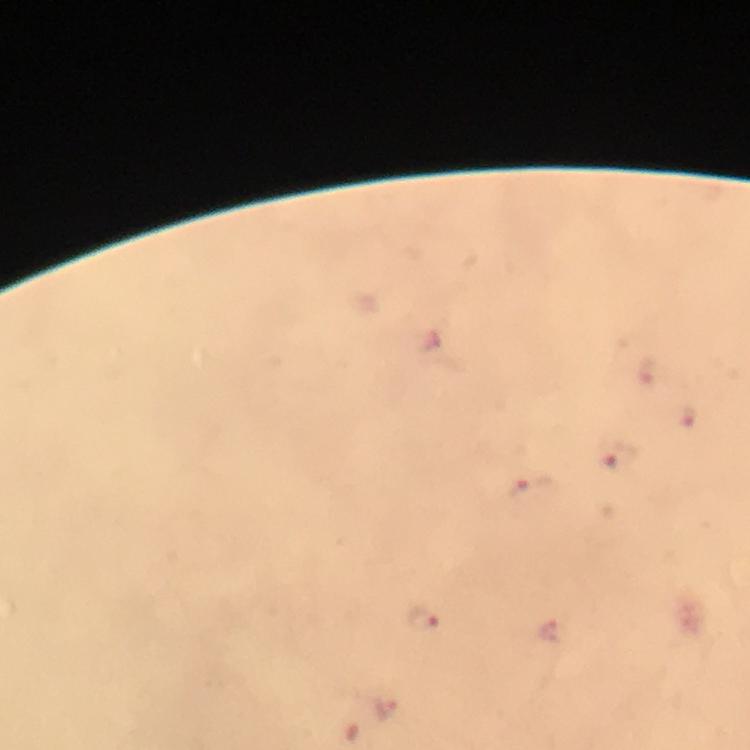

context = from a malaria diagnostic workup
magnification = 100x
capture = smartphone mounted on the microscope
image size = 750×750 pixels
immersion oil = applied
preparation = thick blood smear
cropped from = a single field of view
malaria parasite locations = approximate centers as {x, y} in pixels: {616, 456}, {531, 487}, {422, 619}, {551, 631}, {385, 710}
stain = Giemsa